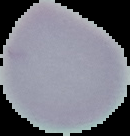

Summary:
  - Image size: 130×136 pixels
  - Preparation: thin blood film
  - Malaria status: uninfected
  - Image type: segmented cell region with the area outside set to black